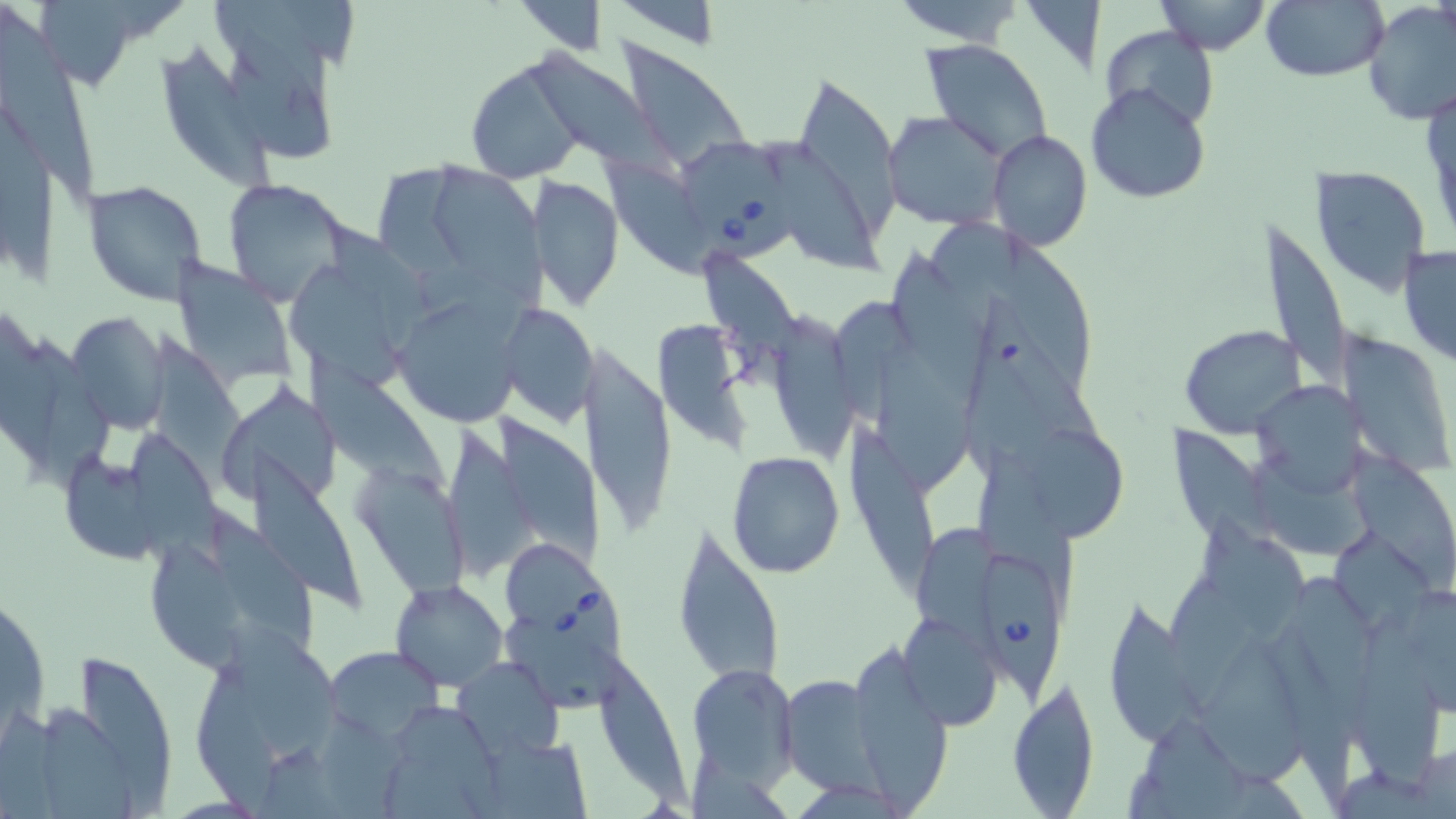

slide-level diagnosis = Babesia divergens
preparation = thin blood film
magnification = 1000x
stain = May-Grünwald-Giemsa
image size = 1456×819 pixels
Babesia divergens-infected red blood cell locations = approximate bounding boxes as (x1,y1)-(x2,y2) corner pairs in pixels: (682,138)-(805,266), (502,547)-(630,669), (978,553)-(1068,706)
uninfected red blood cell locations = approximate bounding boxes as (x1,y1)-(x2,y2) corner pairs in pixels: (514,0)-(608,53), (887,0)-(1028,47), (1151,0)-(1274,54), (1260,1)-(1389,83), (1361,1)-(1456,126), (1016,2)-(1107,73), (0,5)-(98,206), (1101,26)-(1219,130), (615,30)-(756,182), (922,41)-(1054,164), (153,44)-(282,206), (521,45)-(689,188), (229,52)-(341,169), (464,57)-(591,182), (791,67)-(903,240), (1087,83)-(1212,203), (883,110)-(1008,232), (988,129)-(1092,251), (773,140)-(890,283), (439,155)-(541,312), (592,156)-(719,275), (376,166)-(488,287), (1309,166)-(1433,297), (530,175)-(625,312), (220,177)-(353,305), (83,179)-(207,308), (1253,212)-(1353,402), (927,213)-(1031,361), (1002,235)-(1101,408), (1397,244)-(1456,370), (171,255)-(297,382), (703,256)-(821,374), (285,266)-(410,393), (398,294)-(524,435), (964,294)-(1111,473), (503,303)-(600,427), (65,312)-(169,437), (777,315)-(864,460), (653,320)-(752,451), (1178,324)-(1309,438), (152,331)-(257,498), (1338,332)-(1453,480), (22,336)-(117,491), (578,339)-(676,544), (868,340)-(978,502), (307,353)-(455,504), (1250,381)-(1371,496), (217,387)-(351,518), (494,412)-(611,575), (435,423)-(542,578), (842,425)-(942,601), (1026,428)-(1130,546), (126,429)-(233,572), (1168,429)-(1286,577), (980,449)-(1076,623), (1352,450)-(1456,594), (248,451)-(362,611), (726,451)-(845,578), (68,456)-(165,565), (1243,456)-(1386,568), (352,457)-(479,616), (921,515)-(1005,646), (1198,517)-(1307,643), (671,523)-(787,691), (1328,533)-(1442,646), (151,540)-(252,676), (1161,570)-(1270,717), (1291,574)-(1389,723), (390,578)-(507,690), (1103,597)-(1201,749), (900,615)-(1003,729), (223,619)-(353,771), (502,624)-(642,710), (1355,624)-(1442,806), (1195,632)-(1313,792), (591,644)-(698,816), (323,646)-(446,743), (850,648)-(951,813), (81,653)-(178,819), (453,656)-(564,763), (191,659)-(288,819), (686,661)-(798,788), (779,675)-(885,794), (1008,676)-(1100,818), (43,701)-(139,819), (401,706)-(510,819), (1140,714)-(1251,819), (459,737)-(596,819), (1411,743)-(1454,815)
modality = light microscopy
field of view = one of a larger specimen